Report the malaria status of this cell.
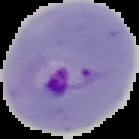
It is parasitized.

Summary:
  - Preparation: thin blood film
  - Image type: segmented cell region on a black background
  - Image size: 139×139 pixels